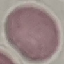

Result: no malaria parasites seen. Acquired by smartphone through the microscope eyepiece. Cell patch, automatically extracted from a larger field of view and resized to 64 × 64 pixels. Thin smear of blood. Giemsa stain.